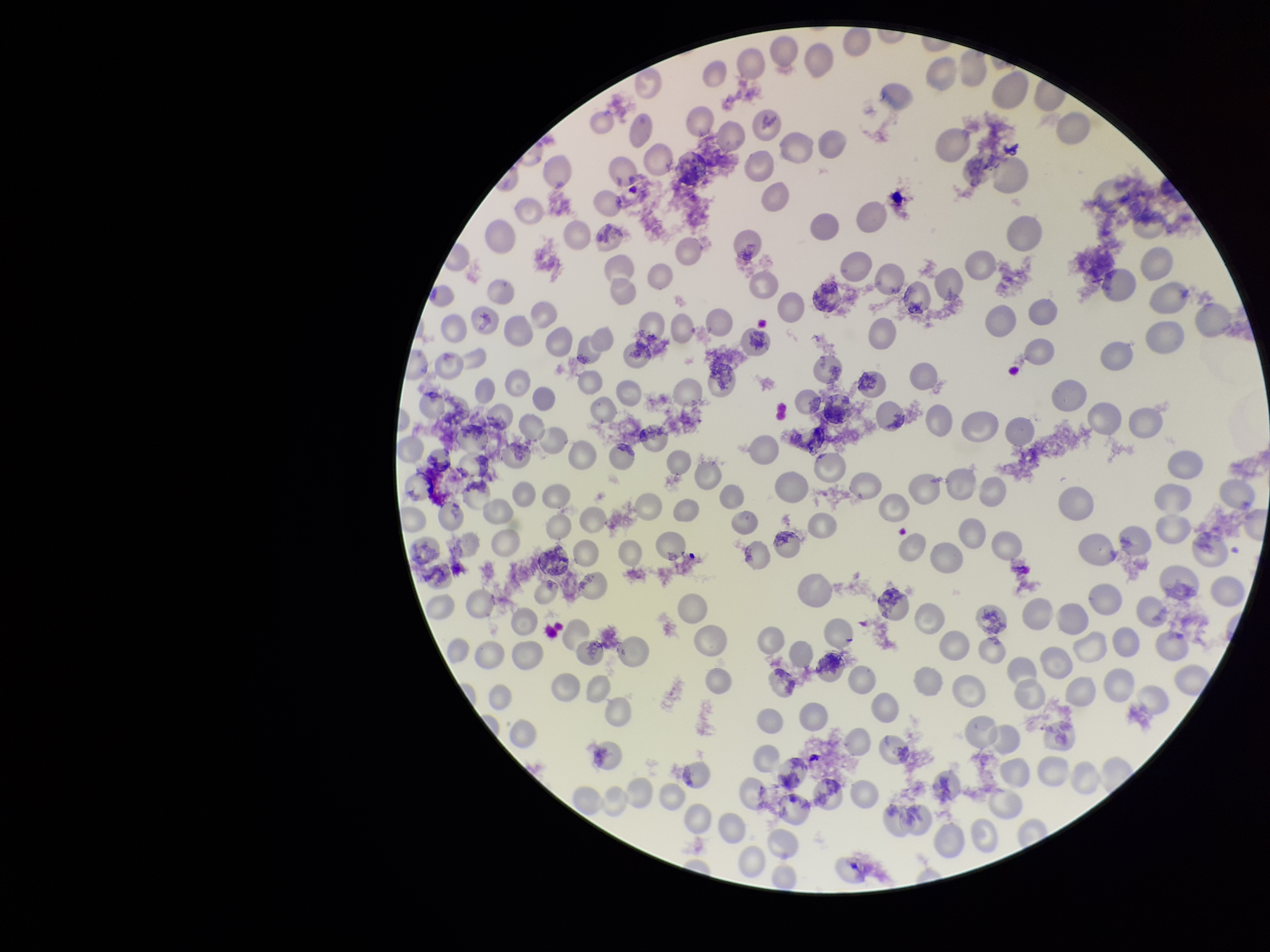
Summary:
  - Patient malaria status: positive
  - Parasitized red blood cells: none identified
  - Preparation: thin blood smear
  - Stain: Giemsa
  - Parasitized red blood cell count: 0
  - Species reported for this patient: Plasmodium vivax
  - Red blood cell count: 213
  - Field of view: one from this slide
  - Image size: 1270×952 pixels
  - Capture: smartphone photograph through the microscope eyepiece